Give the extent of all uninfected red blood cells.
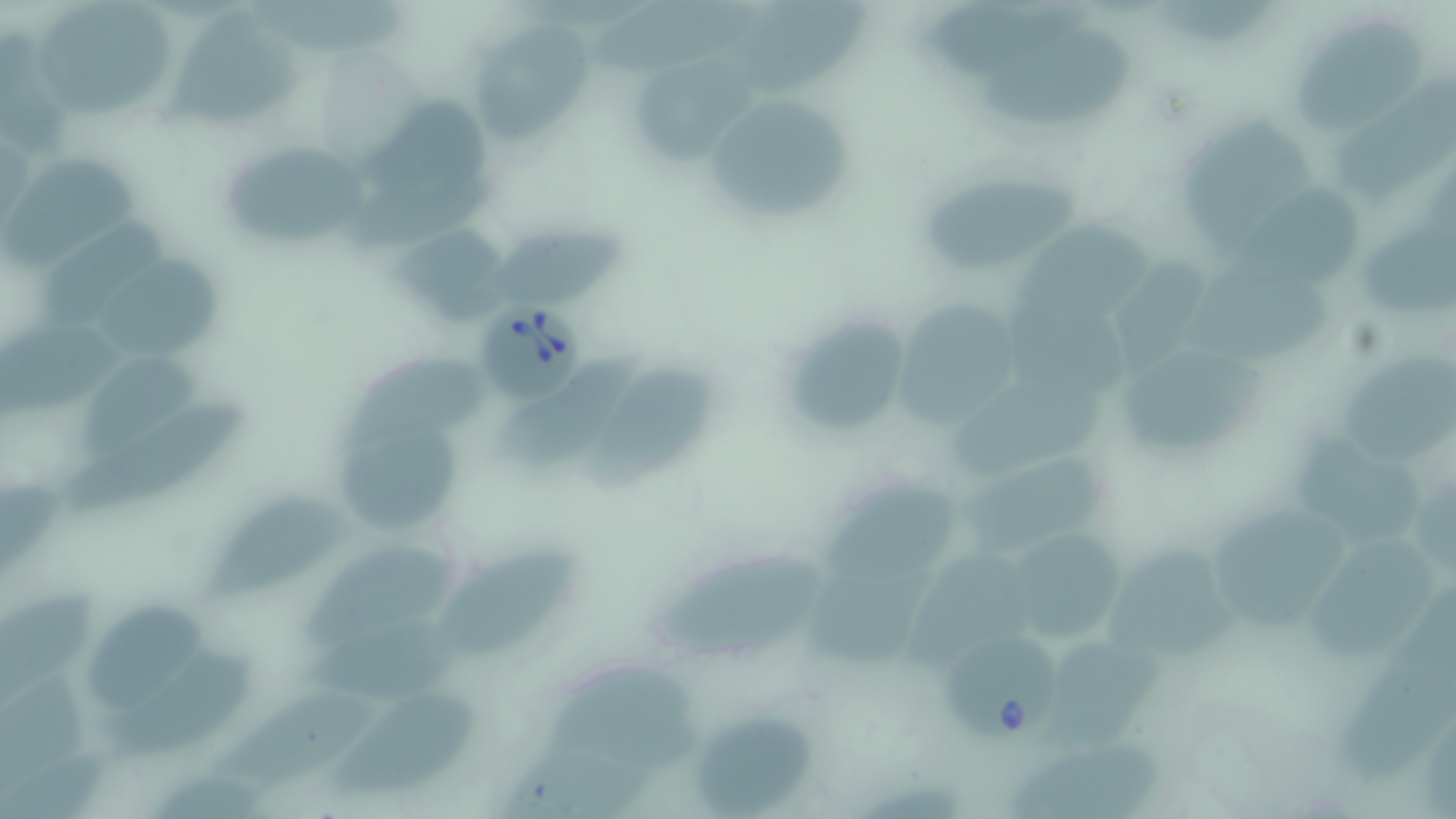
Approximate bounding boxes as [x1, y1, x2, y2] in pixels.
Uninfected red blood cells: [256, 0, 414, 61], [589, 0, 753, 81], [1169, 0, 1274, 44], [731, 2, 870, 98], [926, 3, 1090, 81], [46, 6, 176, 128], [174, 18, 310, 125], [1299, 21, 1433, 128], [1, 29, 76, 157], [989, 29, 1144, 129], [485, 34, 597, 144], [635, 56, 755, 164], [1334, 82, 1455, 210], [713, 88, 857, 219], [362, 89, 499, 188], [1181, 117, 1311, 261], [225, 135, 370, 234], [5, 155, 135, 262], [925, 172, 1090, 271], [354, 175, 509, 247], [1241, 194, 1358, 270], [43, 216, 174, 324], [1034, 216, 1157, 302], [492, 220, 634, 302], [370, 226, 485, 313], [1362, 232, 1455, 316], [113, 258, 229, 347], [1126, 258, 1219, 361], [1200, 278, 1333, 357], [1016, 287, 1141, 399], [904, 304, 1012, 430], [3, 313, 149, 418], [798, 317, 906, 430], [515, 351, 650, 458], [1345, 352, 1456, 462], [1130, 354, 1266, 455], [82, 357, 205, 447], [342, 360, 493, 448], [587, 367, 723, 493], [957, 381, 1101, 474], [76, 396, 247, 501], [343, 420, 477, 519], [1295, 434, 1412, 541], [980, 455, 1114, 557], [1, 477, 67, 577], [828, 485, 967, 574], [1409, 490, 1451, 569], [208, 497, 350, 595], [1217, 511, 1347, 635], [1024, 523, 1125, 629], [1321, 536, 1436, 654], [316, 537, 467, 639], [436, 542, 576, 651], [1114, 545, 1241, 639], [656, 553, 826, 654], [912, 560, 1018, 664], [806, 566, 917, 667], [3, 586, 102, 699], [1334, 596, 1456, 782], [96, 605, 208, 696], [1058, 621, 1169, 731], [312, 623, 487, 688], [114, 651, 257, 758], [551, 662, 693, 758], [3, 672, 94, 792], [342, 679, 483, 789], [224, 683, 386, 767], [692, 714, 820, 816], [1011, 738, 1173, 817], [503, 749, 652, 817], [0, 751, 105, 818], [149, 763, 259, 819].

Summary:
  - Babesia divergens-infected red blood cell locations: [480, 299, 586, 404], [945, 632, 1064, 742]
  - Slide-level diagnosis: Babesia divergens
  - Field of view: single
  - Magnification: 1000x
  - Modality: optical microscopy
  - Stain: May-Grünwald-Giemsa
  - Image size: 1456×819 pixels
  - Preparation: thin blood film